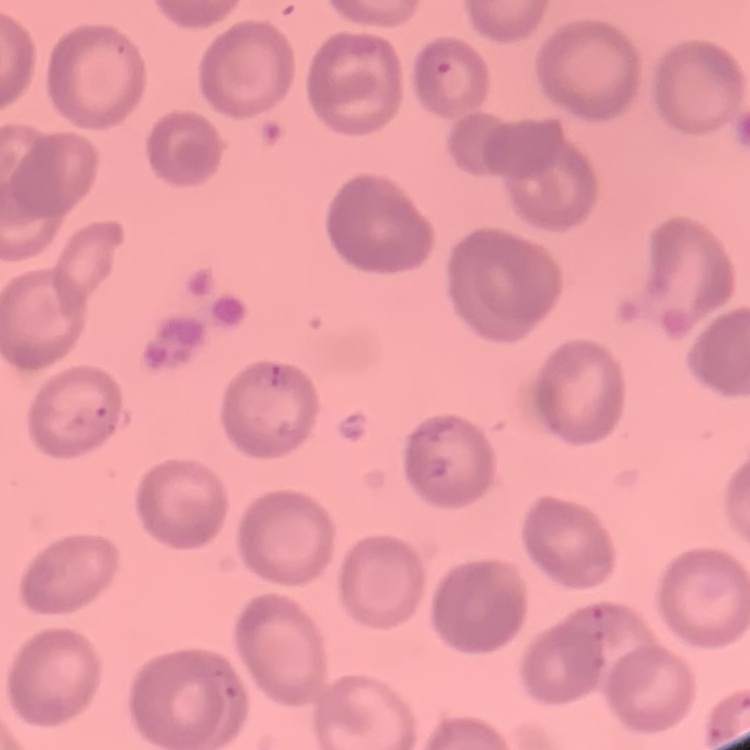
erythrocyte_morphology: no rouleaux formation
image_type: square crop of a larger photomicrograph
stain: Field's or Giemsa
preparation: thin blood smear